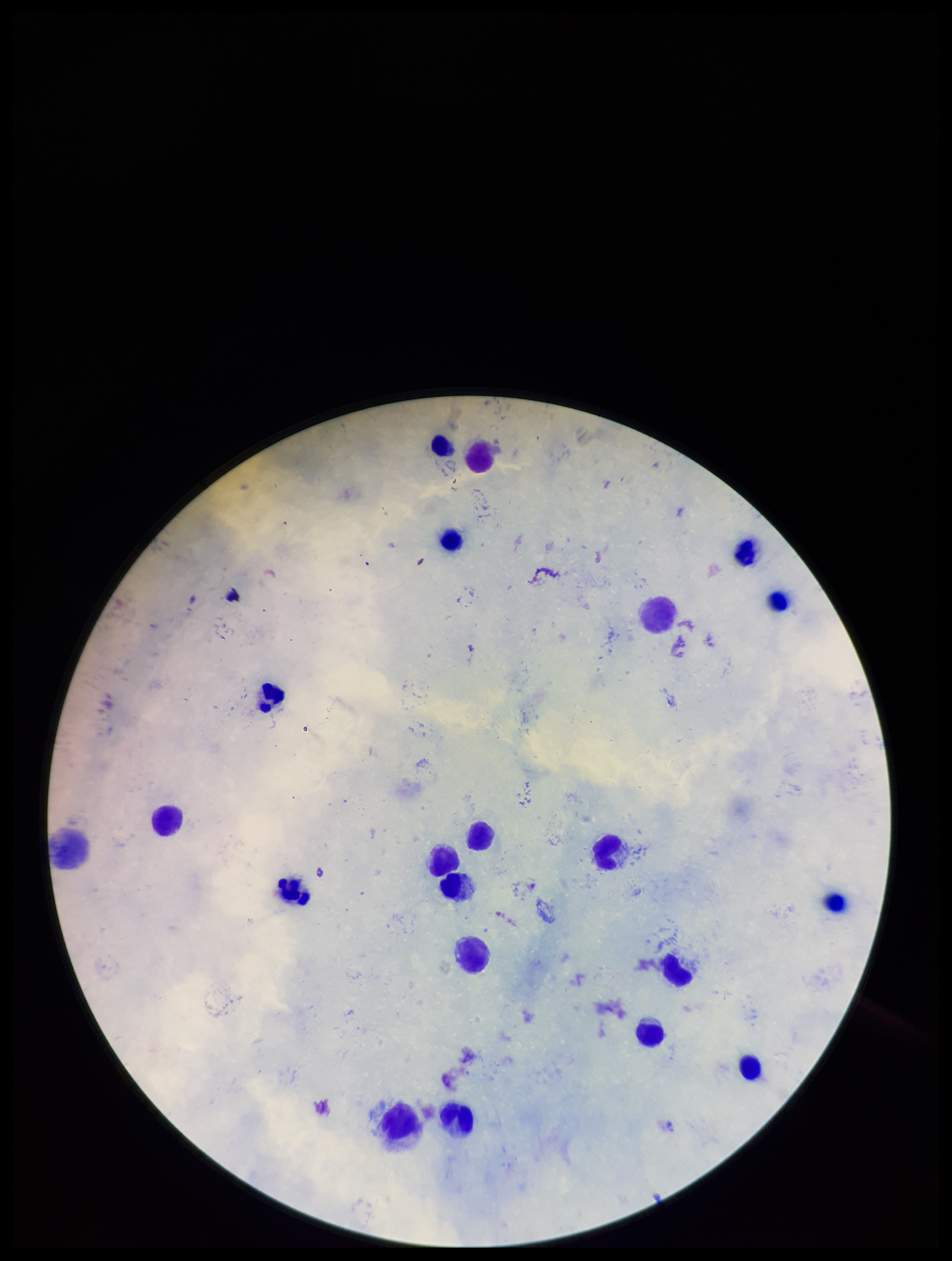
field of view = one from this slide
preparation = thick smear
species reported for this patient = Plasmodium falciparum
image size = 952×1261 pixels
capture = smartphone photograph through the microscope eyepiece
parasite count = 0
Plasmodium parasites = none detected
leukocyte count = 20
stain = Giemsa
patient malaria status = positive